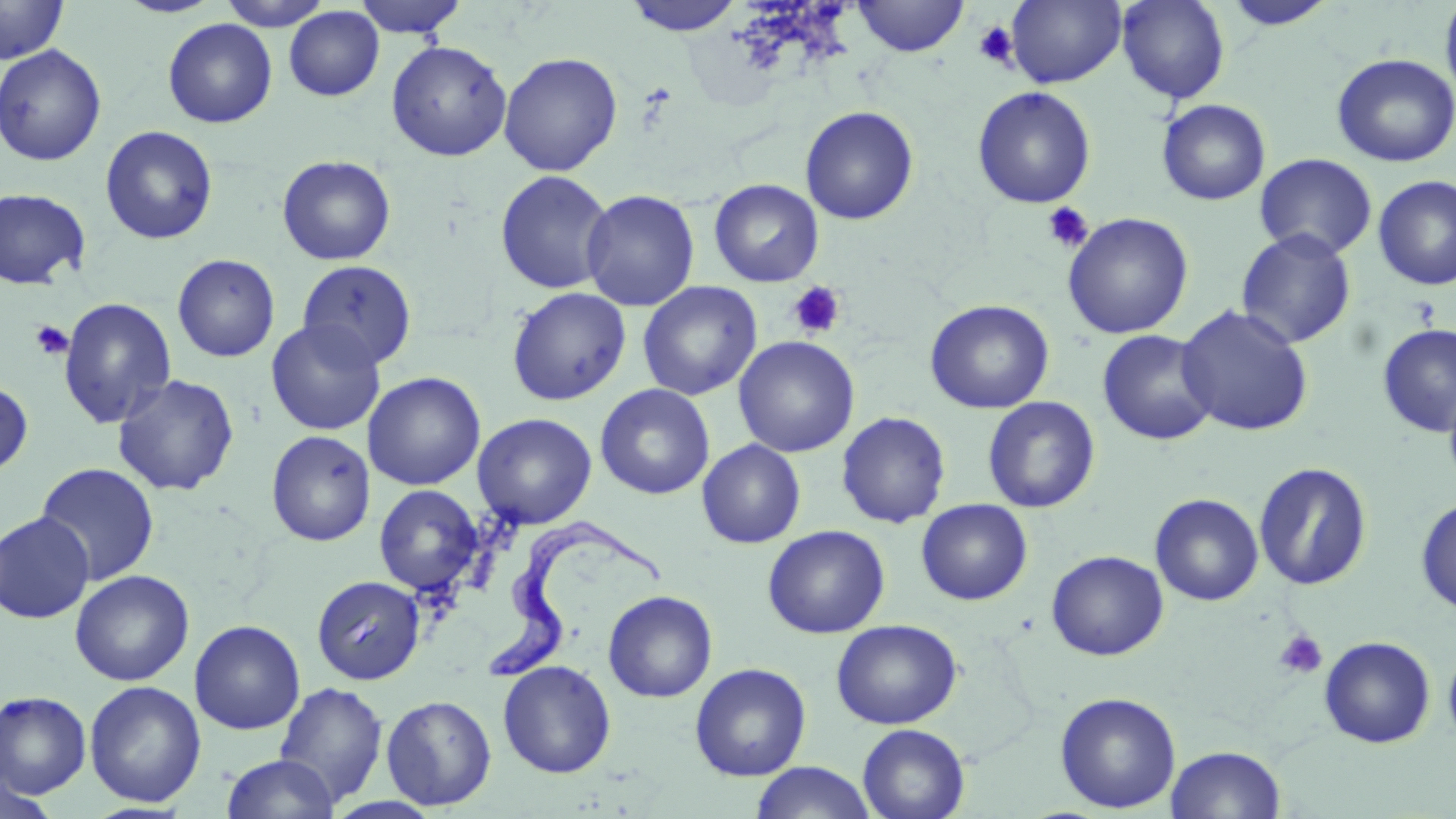

{
  "slide_level_diagnosis": "Trypanosoma brucei",
  "modality": "light microscopy",
  "uninfected_red_blood_cell_locations": "approximate bounding boxes as (x1, y1, x2, y2) in pixels: (114, 0, 226, 18), (218, 0, 333, 30), (352, 0, 468, 38), (621, 0, 745, 36), (851, 0, 970, 57), (1006, 0, 1127, 87), (1116, 0, 1230, 104), (1440, 0, 1456, 108), (0, 1, 68, 64), (1221, 1, 1338, 31), (284, 6, 384, 101), (163, 18, 278, 128), (386, 40, 512, 161), (0, 44, 106, 166), (498, 52, 622, 176), (1331, 53, 1456, 167), (972, 86, 1096, 208), (1156, 99, 1270, 205), (800, 106, 919, 225), (100, 125, 218, 244), (1254, 153, 1377, 260), (277, 155, 396, 266), (494, 169, 615, 295), (1373, 175, 1456, 290), (708, 179, 824, 287), (0, 188, 91, 290), (581, 189, 700, 312), (1062, 212, 1194, 340), (1235, 228, 1357, 349), (172, 254, 280, 363), (297, 259, 417, 371), (637, 281, 761, 401), (506, 287, 631, 406), (57, 297, 177, 429), (925, 299, 1054, 414), (1176, 304, 1314, 436), (265, 319, 386, 435), (1376, 323, 1456, 438), (1097, 329, 1218, 446), (733, 335, 859, 457), (362, 372, 486, 490), (112, 373, 240, 496), (0, 378, 34, 478), (1443, 380, 1456, 496), (595, 383, 715, 500), (982, 396, 1100, 513), (836, 411, 952, 528), (472, 413, 597, 529), (266, 430, 376, 546), (697, 439, 806, 548), (1253, 461, 1373, 590), (35, 462, 160, 585), (373, 485, 483, 596), (1150, 493, 1264, 606), (1415, 497, 1456, 615), (916, 499, 1033, 605), (0, 512, 95, 624), (762, 524, 890, 638), (1046, 550, 1168, 660), (70, 570, 194, 686), (311, 575, 426, 684), (603, 590, 717, 702), (831, 619, 961, 729), (189, 620, 305, 735), (1319, 636, 1436, 748), (1442, 641, 1456, 750), (498, 660, 616, 778), (689, 662, 811, 781), (84, 680, 207, 807), (273, 682, 389, 808), (0, 691, 91, 798), (1054, 692, 1181, 813), (381, 694, 497, 810), (857, 723, 970, 819), (1165, 745, 1286, 818), (221, 753, 339, 819), (750, 762, 877, 819), (0, 772, 62, 819)",
  "image_size": "1456×819 pixels",
  "preparation": "thin blood smear",
  "field_of_view": "one of a larger specimen",
  "trypanosoma_brucei_locations": "approximate bounding boxes as (x1, y1, x2, y2) in pixels: (489, 520, 663, 682)",
  "magnification": "1000x",
  "stain": "May-Grünwald-Giemsa",
  "platelet_locations": "approximate bounding boxes as (x1, y1, x2, y2) in pixels: (973, 21, 1018, 68), (1041, 202, 1094, 253), (787, 281, 846, 339), (30, 320, 74, 361), (1273, 629, 1328, 680)"
}